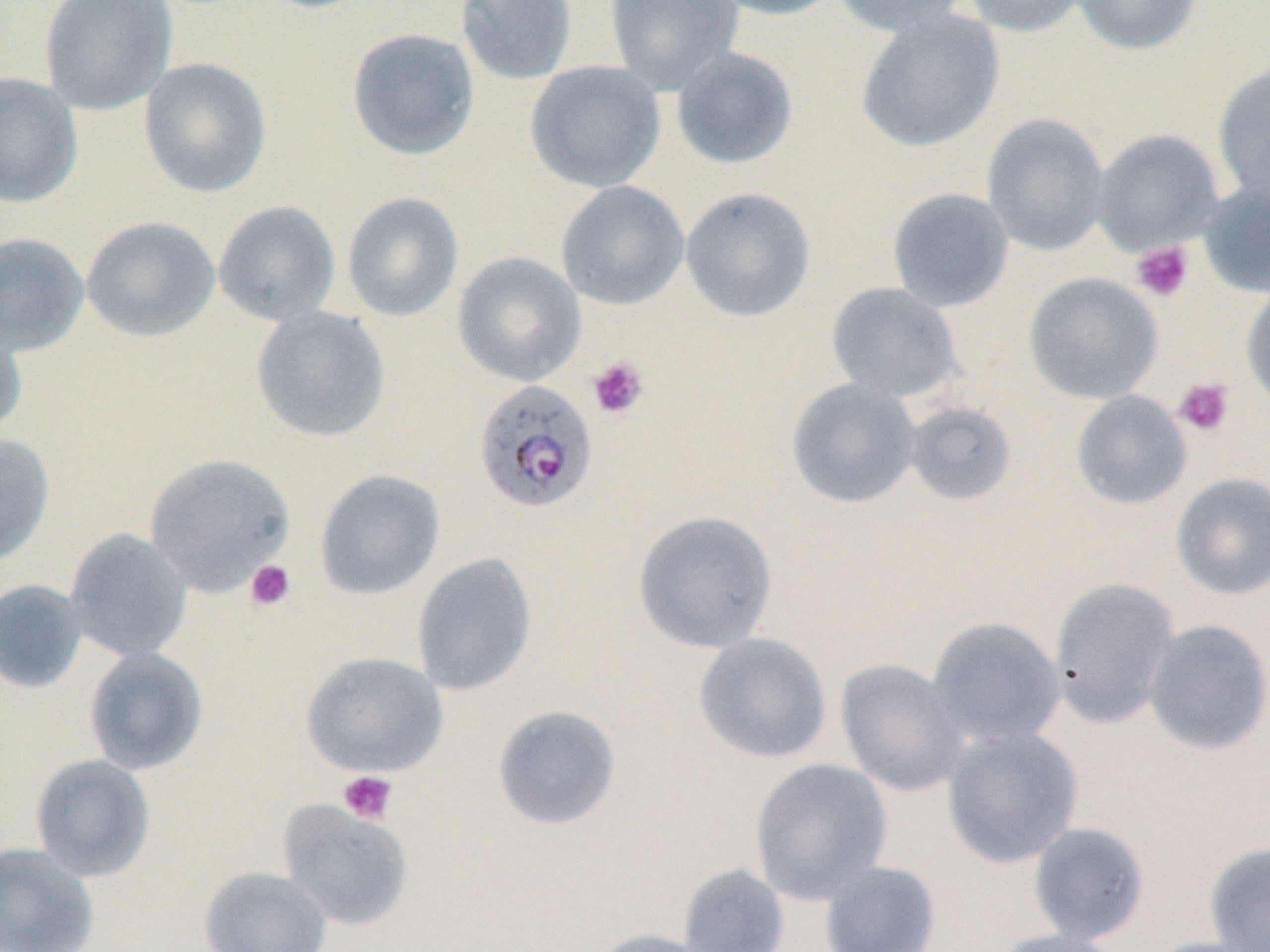

Approximate bounding boxes as (x1, y1, x2, y2) in pixels. Uninfected red blood cell locations (subset): (38, 0, 177, 115), (455, 0, 578, 86), (604, 0, 744, 94), (704, 0, 845, 21), (831, 0, 970, 37), (960, 0, 1091, 38), (1071, 0, 1202, 56), (854, 8, 1005, 153), (346, 27, 480, 161), (669, 46, 799, 170), (138, 58, 272, 198), (524, 60, 666, 193), (1212, 62, 1270, 201), (0, 73, 83, 209), (981, 113, 1110, 256), (1090, 128, 1224, 254), (1197, 176, 1270, 298), (556, 180, 690, 311), (680, 187, 816, 322), (886, 187, 1015, 312), (341, 191, 464, 323), (213, 200, 342, 327), (81, 216, 221, 342), (0, 232, 90, 357), (452, 251, 586, 387), (1022, 272, 1163, 405), (825, 281, 963, 402), (1240, 282, 1270, 412), (251, 306, 391, 443), (0, 317, 28, 440), (786, 376, 922, 509), (1070, 389, 1193, 511), (903, 400, 1018, 507), (0, 433, 55, 566), (144, 452, 295, 595), (314, 469, 445, 600), (1169, 472, 1270, 601), (632, 510, 779, 654), (64, 529, 192, 663), (410, 552, 538, 697), (1048, 576, 1179, 729), (0, 578, 87, 694), (926, 616, 1066, 748), (1142, 619, 1270, 756), (693, 633, 832, 764), (83, 647, 208, 775), (299, 651, 450, 778), (835, 658, 970, 797), (491, 704, 622, 830), (941, 727, 1083, 868), (29, 753, 156, 882), (749, 758, 893, 904), (1027, 821, 1150, 944), (0, 841, 99, 952), (1204, 843, 1270, 952), (819, 860, 941, 952), (678, 863, 790, 952), (199, 865, 333, 952), (587, 928, 723, 952), (988, 928, 1128, 952), (1144, 937, 1266, 952). Plasmodium falciparum-infected red blood cell locations: (473, 379, 598, 514). Platelet locations (subset): (1130, 241, 1194, 303), (587, 356, 649, 419), (1173, 377, 1235, 437), (245, 560, 296, 611), (338, 770, 398, 825). Slide-level diagnosis: Plasmodium falciparum. Light microscopy. 1000x magnification. One field of a larger specimen. Image is 1270×952 pixels. May-Grünwald-Giemsa stain. Thin blood film.